Evaluate for Plasmodium parasites.
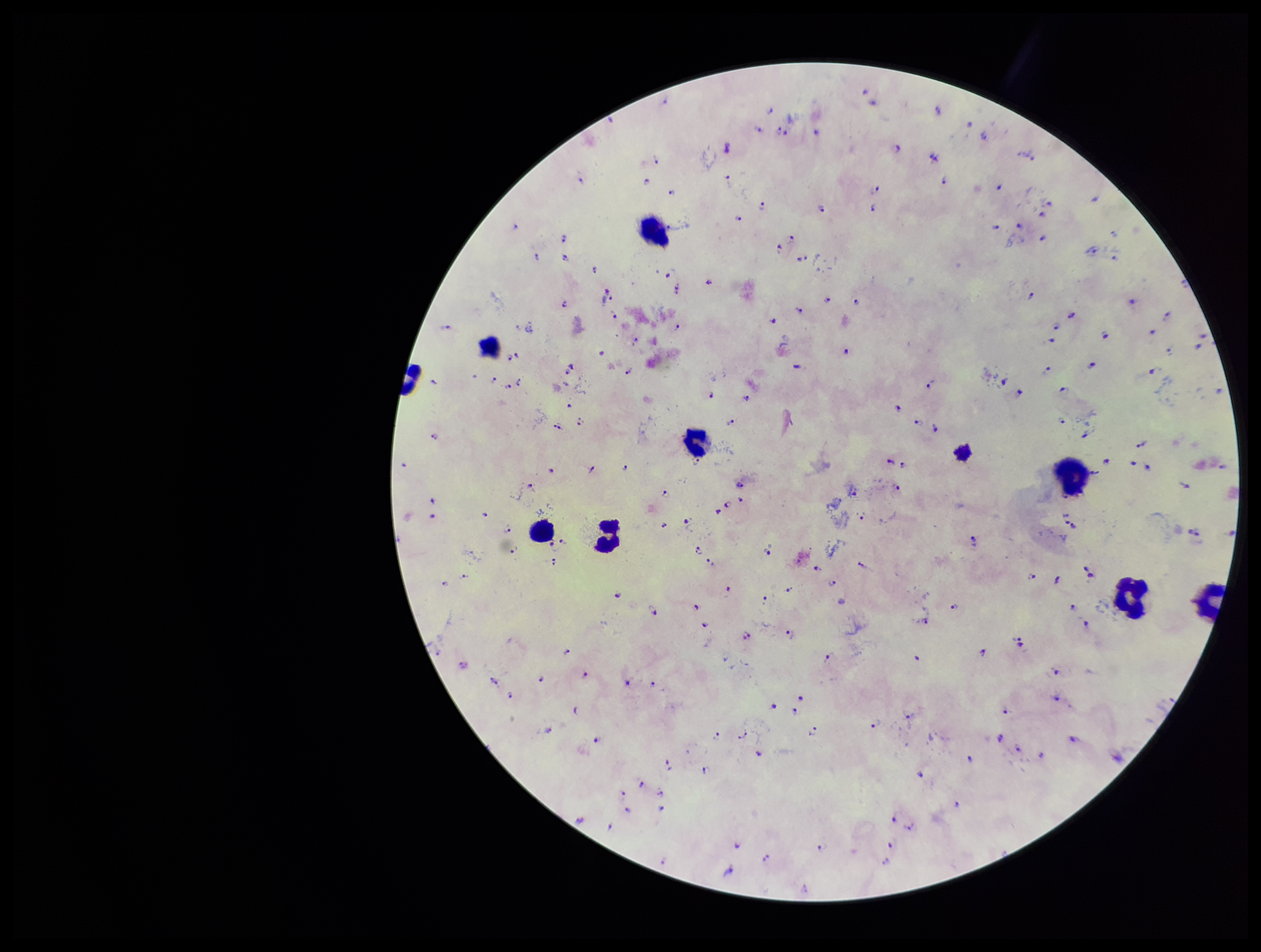

Detected.

Summary:
  - Parasite count: 159
  - Species reported for this patient: Plasmodium falciparum
  - Preparation: thick blood smear
  - Stain: Giemsa
  - Image size: 1261×952 pixels
  - Leukocyte count: 9
  - Field of view: one from this slide
  - Capture: smartphone photograph through the microscope eyepiece
  - Patient malaria status: positive